Classify this cell by malaria status.
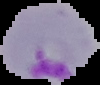

It is parasitized.

Summary:
  - Preparation: thin blood film
  - Image size: 100×85 pixels
  - Image type: cell region segmented out of the field of view; surrounding area masked to black